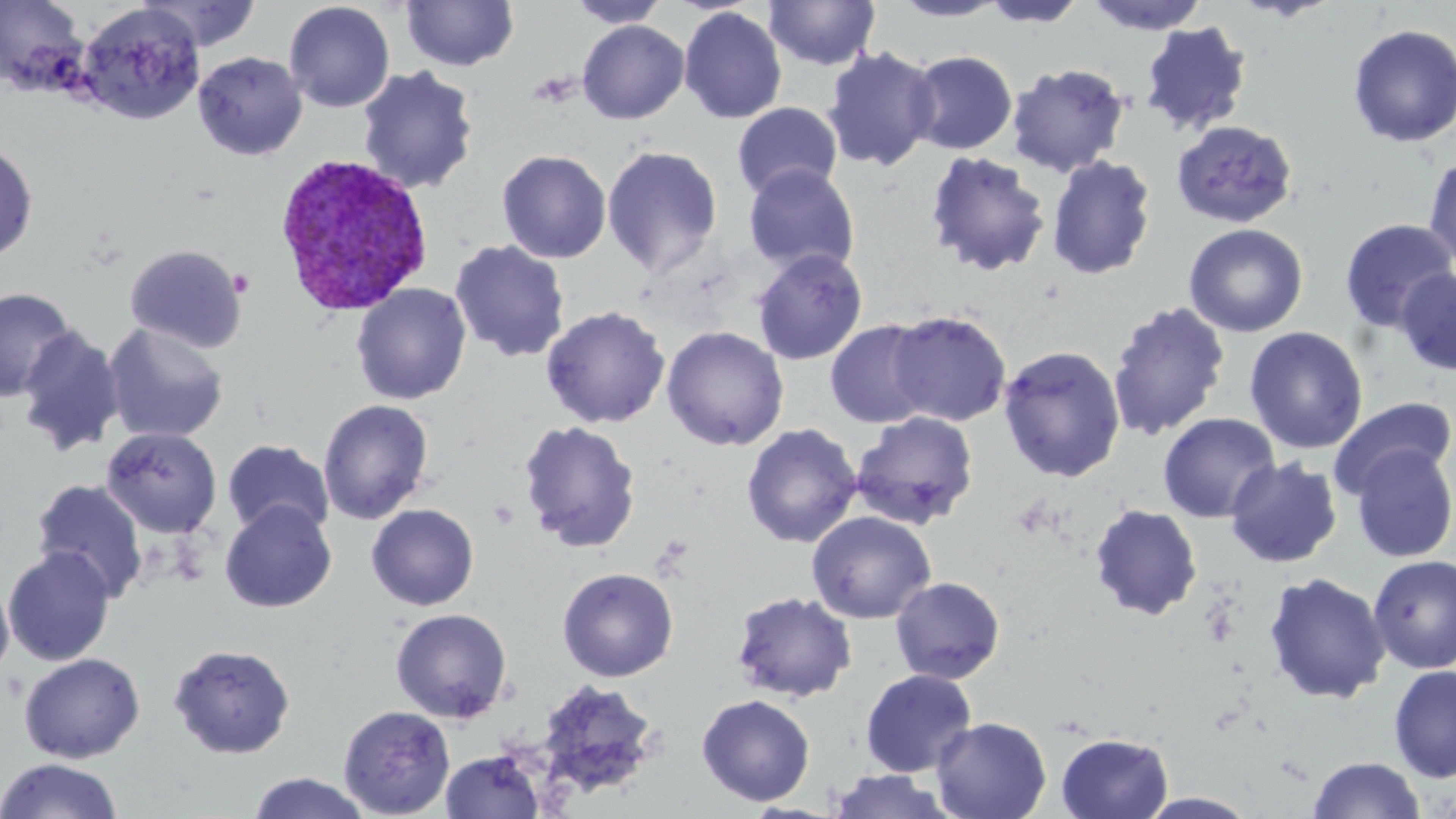 Approximate bounding boxes as (x1,y1)-(x2,y2) corner pairs in pixels. Plasmodium vivax-infected red blood cell locations: (271,152)-(435,317). Platelet locations: (489,498)-(520,529), (1202,603)-(1240,648). Uninfected red blood cell locations: (0,0)-(88,94), (566,0)-(670,28), (890,0)-(1009,21), (136,1)-(263,52), (283,1)-(395,113), (401,1)-(519,71), (764,1)-(881,71), (980,1)-(1086,29), (1081,1)-(1212,35), (76,3)-(206,125), (678,6)-(787,124), (577,20)-(689,124), (1139,21)-(1253,137), (1347,23)-(1456,148), (822,46)-(940,172), (907,50)-(1018,155), (193,51)-(307,160), (1006,62)-(1130,177), (356,65)-(480,195), (732,102)-(842,201), (1171,120)-(1298,228), (0,139)-(38,263), (601,145)-(723,279), (497,149)-(612,263), (924,149)-(1052,278), (1423,151)-(1456,269), (1047,155)-(1157,280), (743,164)-(859,277), (1338,217)-(1456,333), (1184,223)-(1308,337), (449,240)-(569,362), (125,243)-(248,353), (752,249)-(868,365), (1395,267)-(1456,376), (351,283)-(471,405), (0,285)-(78,402), (1108,301)-(1231,441), (540,305)-(670,428), (888,310)-(1012,426), (825,319)-(935,428), (102,322)-(229,444), (661,326)-(789,451), (1245,326)-(1367,454), (17,327)-(125,458), (998,345)-(1127,483), (1329,396)-(1456,499), (318,398)-(434,524), (849,411)-(979,530), (1158,412)-(1280,523), (518,420)-(641,552), (741,423)-(862,548), (101,426)-(222,538), (221,439)-(335,538), (1348,443)-(1456,563), (1225,457)-(1343,568), (30,477)-(149,602), (220,500)-(337,613), (366,503)-(479,611), (1089,504)-(1203,620), (807,511)-(936,624), (2,546)-(116,666), (1368,554)-(1456,673), (557,567)-(678,682), (0,571)-(15,685), (1262,571)-(1391,704), (890,576)-(1006,685), (730,591)-(857,703), (390,608)-(513,724), (168,643)-(296,758), (18,651)-(146,763), (1388,664)-(1456,782), (860,669)-(977,778), (533,679)-(662,801), (696,694)-(815,806), (338,705)-(455,817), (932,717)-(1051,819), (1055,732)-(1174,818), (440,749)-(546,818), (1307,756)-(1426,818), (0,758)-(124,818), (827,770)-(956,819), (247,772)-(372,819), (1137,792)-(1259,819). Slide-level diagnosis: Plasmodium vivax. Single field of view. Captured at 1000x magnification. May-Grünwald-Giemsa stain. Light microscopy. Thin blood film. Image is 1456×819 pixels.